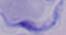

identification = trypanosome
magnification = 1000x
modality = micrograph